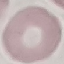
Summary:
  - Malaria status: uninfected
  - Stain: Giemsa
  - Image type: automatically extracted cell patch, resized to 64 × 64 pixels
  - Capture: smartphone camera at the microscope eyepiece
  - Preparation: thin blood smear